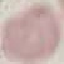
{
  "malaria_status": "uninfected",
  "image_type": "automatically extracted cell patch, resized to 64 × 64 pixels",
  "capture": "smartphone camera at the microscope eyepiece",
  "stain": "Giemsa",
  "preparation": "thin blood film"
}